Classify this cell by malaria status.
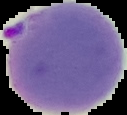

Parasitized.

Summary:
  - Preparation: thin blood smear
  - Image size: 127×115 pixels
  - Image type: cell region segmented out of the field of view; surrounding area masked to black